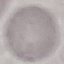

Summary:
  - Malaria status: uninfected
  - Stain: Giemsa
  - Preparation: thin smear
  - Image type: automatically extracted cell patch, resized to 64 × 64 pixels
  - Capture: smartphone through the microscope eyepiece